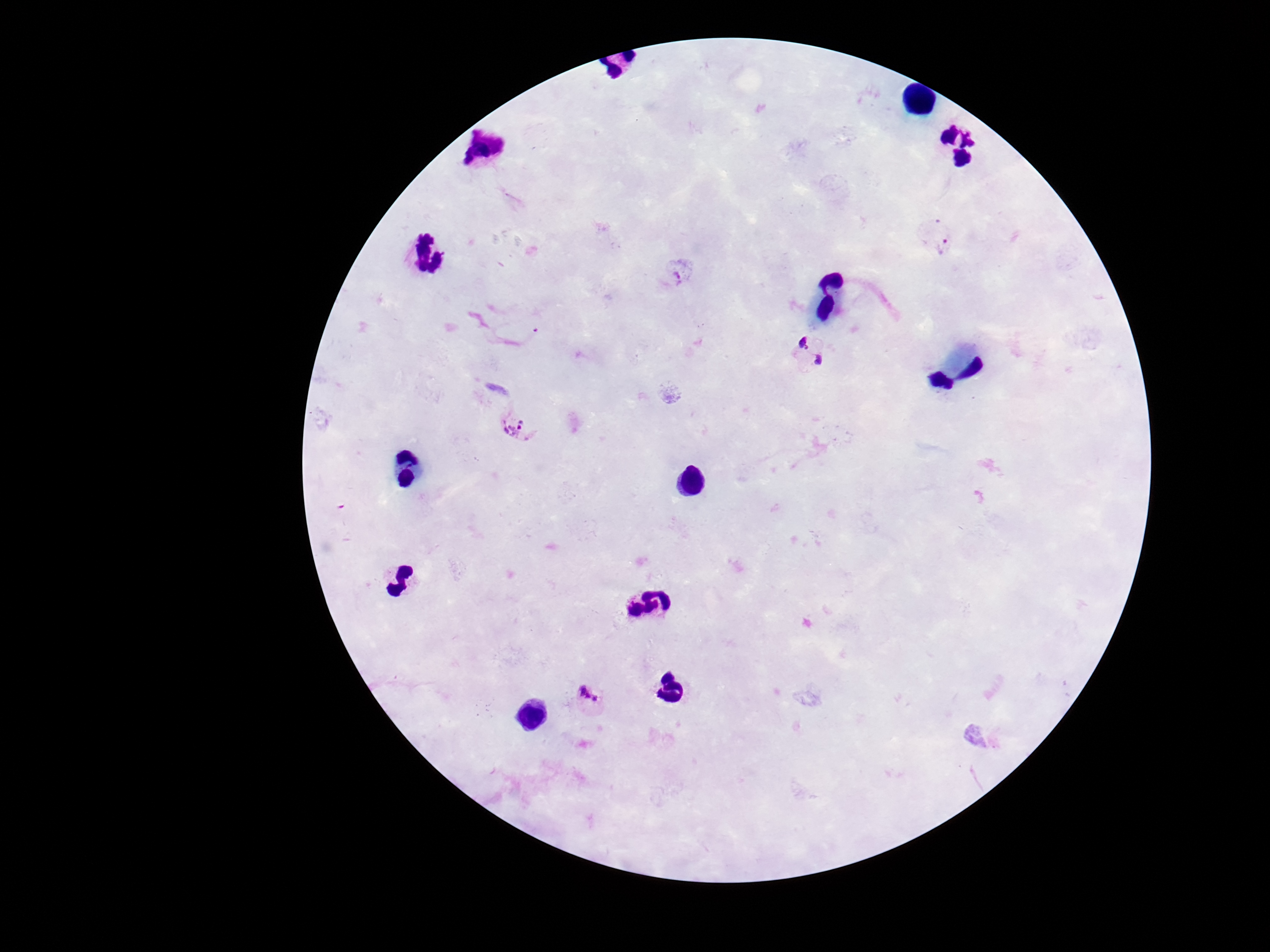
{
  "capture": "smartphone camera through the microscope eyepiece",
  "patient_malaria_status": "positive",
  "preparation": "thick blood film",
  "stain": "Giemsa",
  "plasmodium_parasite_locations": "approximate centers as {x, y} in pixels: {940, 236}, {680, 275}, {809, 352}, {514, 426}, {592, 701}",
  "field_of_view": "one from this slide",
  "image_size": "1270×952 pixels",
  "magnification": "100x"
}